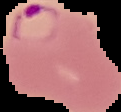

{
  "preparation": "thin blood smear",
  "image_type": "segmented cell region on a black background",
  "image_size": "121×112 pixels",
  "malaria_status": "parasitized"
}